Locate every white blood cell.
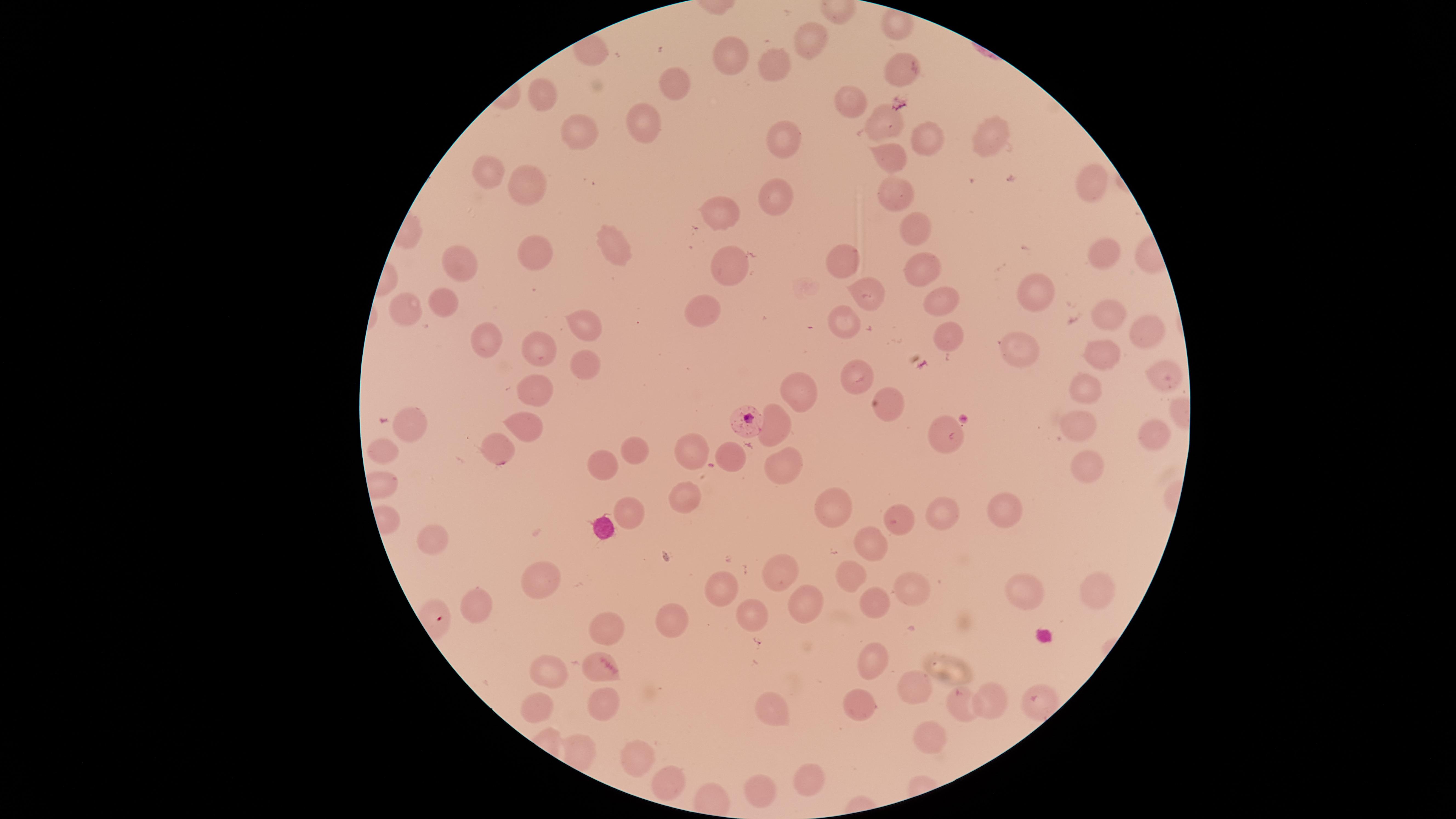
No white blood cells identified.

{
  "image_size": "1456×819 pixels",
  "uninfected_red_blood_cells": "approximate marker points as [x, y] in pixels: [809, 42], [729, 64], [773, 64], [899, 68], [673, 83], [544, 98], [843, 104], [643, 120], [884, 127], [580, 136], [780, 136], [993, 136], [929, 137], [893, 158], [491, 170], [1092, 179], [526, 186], [897, 190], [776, 195], [724, 210], [912, 227], [608, 246], [531, 249], [1102, 253], [843, 258], [453, 260], [725, 267], [924, 268], [865, 293], [941, 296], [1032, 296], [439, 303], [702, 305], [402, 307], [1104, 316], [844, 320], [579, 326], [953, 333], [1144, 333], [482, 338], [534, 345], [1031, 345], [1100, 355], [580, 367], [1156, 372], [860, 378], [1084, 386], [543, 390], [797, 393], [886, 403], [525, 423], [1078, 426], [412, 430], [776, 430], [938, 434], [1149, 435], [495, 448], [632, 449], [695, 450], [381, 457], [728, 463], [783, 466], [1089, 466], [595, 470], [682, 493], [1006, 503], [835, 507], [631, 512], [940, 515], [904, 522], [432, 537], [869, 544], [776, 569], [850, 572], [540, 576], [908, 579], [717, 588], [1017, 590], [1098, 596], [478, 600], [869, 603], [798, 607], [750, 616], [665, 620], [599, 628], [871, 660], [594, 664], [550, 674], [913, 684], [997, 700], [960, 704], [603, 705], [851, 706], [771, 708], [532, 710], [926, 739], [575, 743], [638, 754], [666, 775], [803, 779], [759, 788]",
  "species": "Plasmodium falciparum",
  "visible_region": "circular",
  "preparation": "thin smear of blood",
  "stain": "Giemsa",
  "parasitized_red_blood_cells": "approximate marker points as [x, y] in pixels: [746, 421]",
  "field_of_view": "single",
  "presence": "malaria parasites seen",
  "capture": "smartphone photograph through the microscope eyepiece"
}